Point out each Plasmodium parasite.
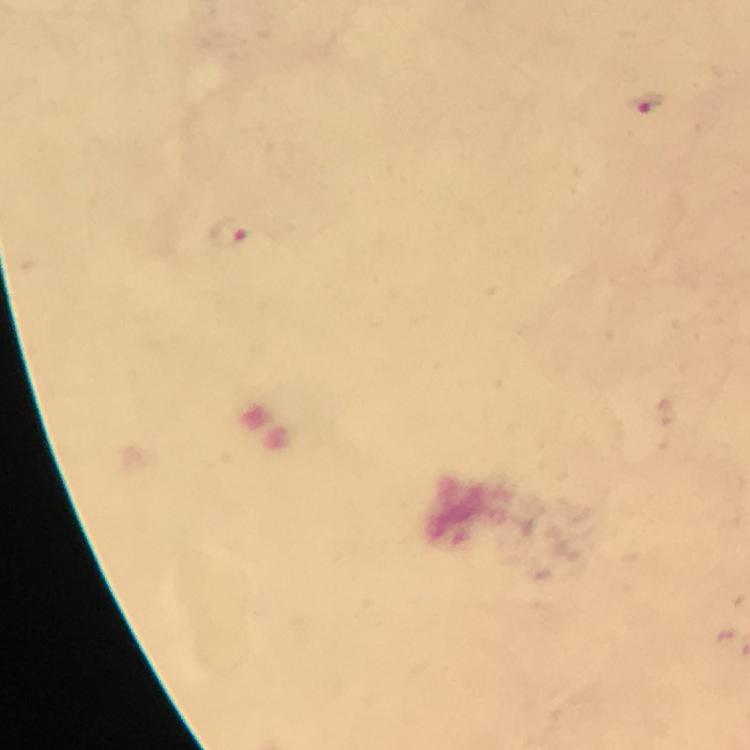
Approximate centers as (x, y) in pixels.
Plasmodium parasites: (647, 104), (229, 235).

Thick smear. Smartphone photograph taken through a microscope. Image is 750×750 pixels. At 100x magnification. From a diagnostic examination for malaria. Giemsa stain. Immersion oil applied. Cropped region of a single field of view.